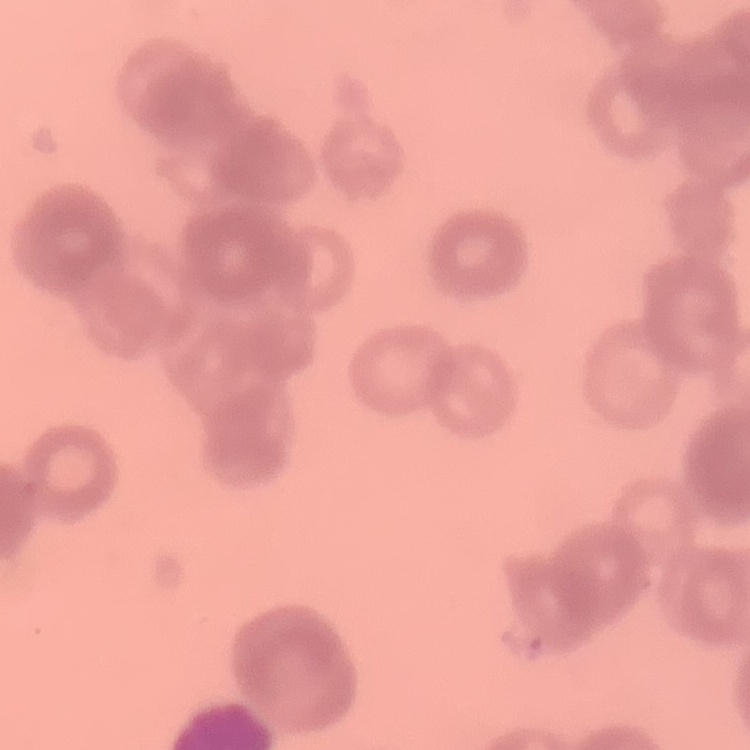

erythrocyte morphology = rouleaux formation
preparation = thin blood smear
stain = Field's or Giemsa
image type = square crop of a larger photomicrograph